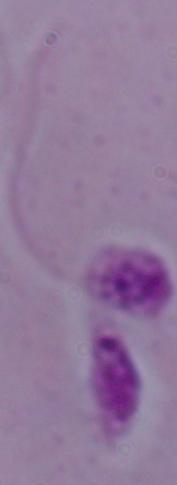
modality = micrograph
magnification = 1000x
identification = Leishmania